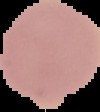

preparation: thin blood smear
image_type: segmented cell region with the area outside set to black
image_size: 100×112 pixels
malaria_status: uninfected